Name the parasite shown.
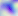

This is Toxoplasma gondii.

Summary:
  - Modality: photomicrograph
  - Magnification: 400x